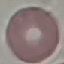
result = negative for malaria parasites
capture = smartphone through the microscope eyepiece
image type = cell patch, automatically extracted from a larger field of view and resized to 64 × 64 pixels
stain = Giemsa
preparation = thin blood film